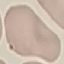

result = no malaria parasites detected
preparation = thin blood smear
stain = Giemsa
capture = smartphone through the microscope eyepiece
image type = automatically extracted cell patch, resized to 64 × 64 pixels